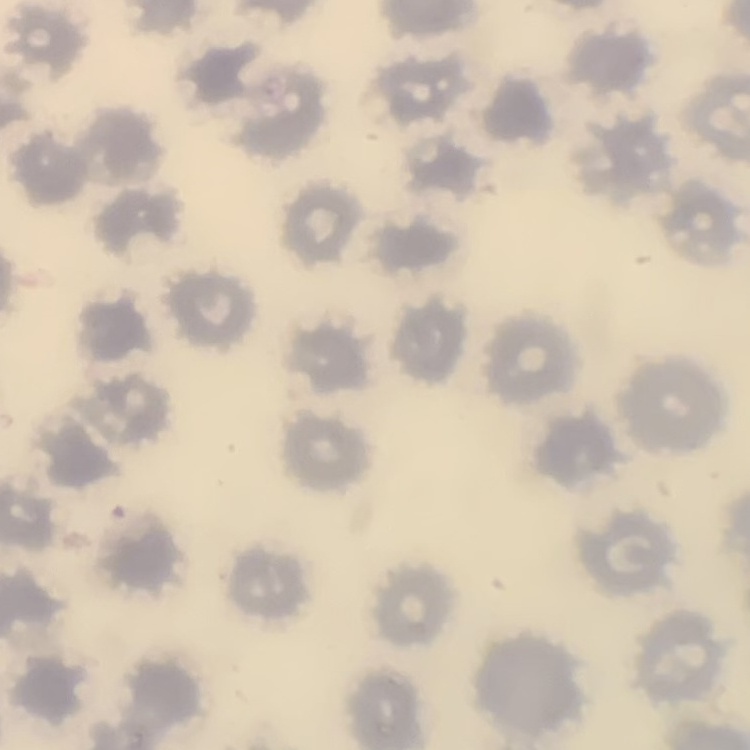
Summary:
  - Erythrocyte morphology: no rouleaux formation
  - Stain: Field's or Giemsa
  - Image type: one tile cut from a larger photomicrograph
  - Preparation: thin blood smear